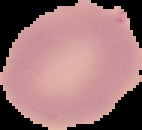
image size = 142×130 pixels
image type = segmented cell region with the area outside set to black
preparation = thin blood smear
malaria status = uninfected